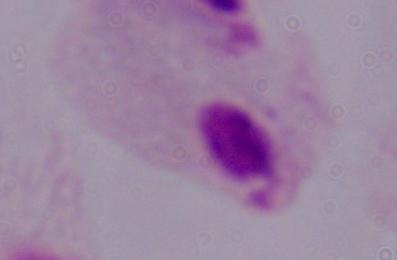

Summary:
  - Modality: photomicrograph
  - Identification: trichomonad
  - Magnification: 1000x